State which cell type is depicted.
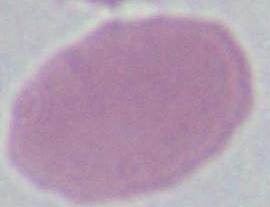
This is an erythrocyte.

Summary:
  - Magnification: 1000x
  - Modality: photomicrograph